Classify this cell by malaria status.
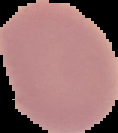

Uninfected.

image type = segmented cell region on a black background
preparation = thin blood film
image size = 118×133 pixels